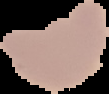
{
  "result": "negative for malaria parasites",
  "image_size": "109×94 pixels",
  "image_type": "cell region segmented out of the field of view; surrounding area masked to black",
  "preparation": "thin blood film"
}